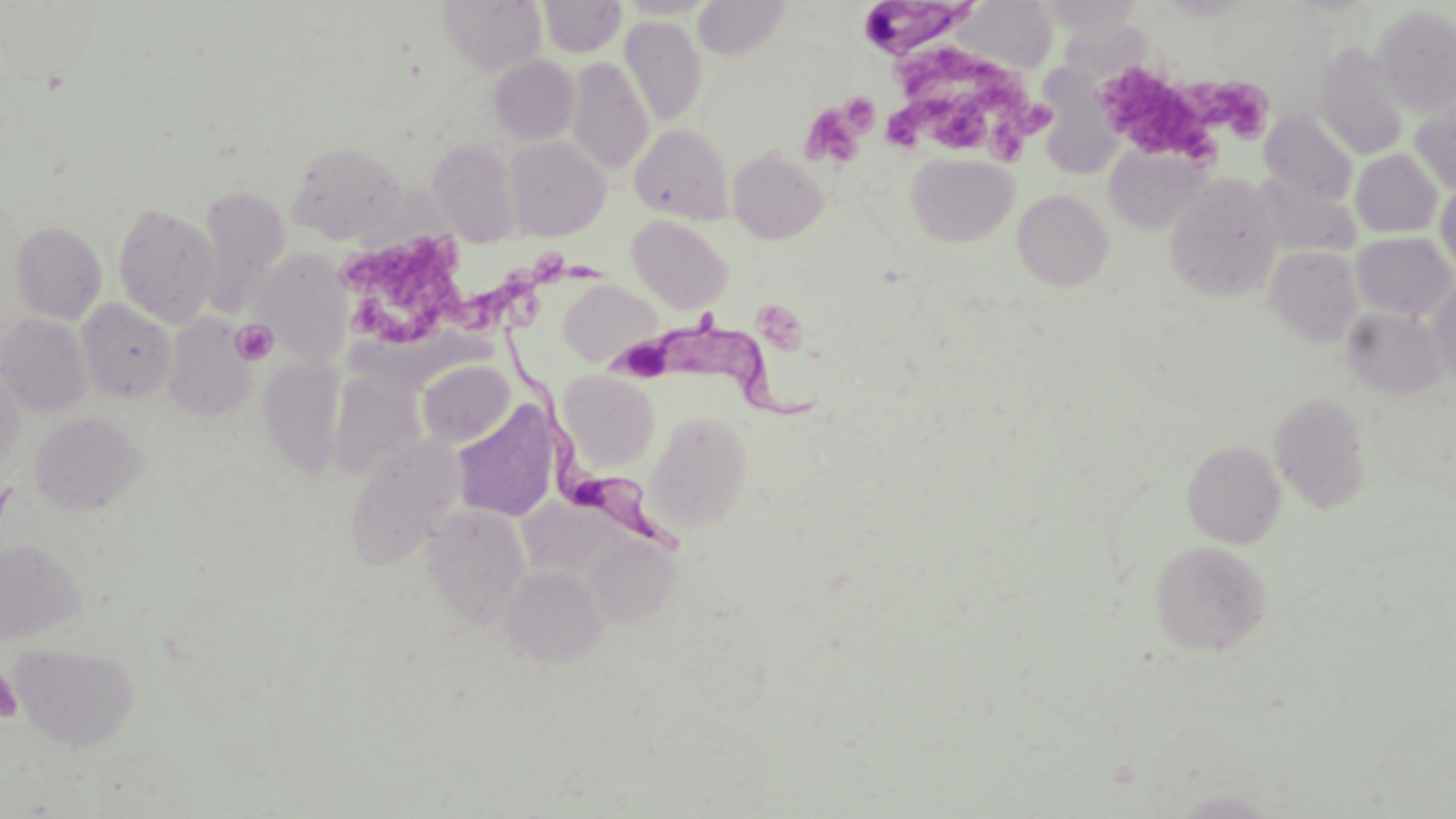
Summary:
  - Coordinate format: approximate bounding boxes as named x1/y1/x2/y2 corners in pixels
  - Uninfected red blood cell locations: (x1=439, y1=0, x2=546, y2=74), (x1=538, y1=0, x2=627, y2=57), (x1=617, y1=0, x2=719, y2=18), (x1=693, y1=0, x2=793, y2=60), (x1=958, y1=0, x2=1057, y2=74), (x1=1039, y1=0, x2=1144, y2=34), (x1=1373, y1=6, x2=1456, y2=116), (x1=620, y1=17, x2=707, y2=125), (x1=1315, y1=44, x2=1409, y2=159), (x1=489, y1=56, x2=580, y2=144), (x1=566, y1=57, x2=654, y2=175), (x1=1039, y1=62, x2=1130, y2=178), (x1=1411, y1=98, x2=1456, y2=193), (x1=1261, y1=110, x2=1359, y2=206), (x1=630, y1=124, x2=734, y2=223), (x1=504, y1=136, x2=610, y2=241), (x1=428, y1=138, x2=522, y2=248), (x1=286, y1=140, x2=408, y2=243), (x1=1105, y1=144, x2=1210, y2=234), (x1=728, y1=148, x2=828, y2=243), (x1=1351, y1=149, x2=1443, y2=237), (x1=907, y1=154, x2=1018, y2=246), (x1=1254, y1=172, x2=1360, y2=257), (x1=1165, y1=174, x2=1282, y2=301), (x1=1435, y1=182, x2=1456, y2=277), (x1=198, y1=185, x2=290, y2=313), (x1=1013, y1=190, x2=1113, y2=291), (x1=112, y1=201, x2=221, y2=328), (x1=627, y1=215, x2=733, y2=314), (x1=10, y1=221, x2=107, y2=324), (x1=1352, y1=232, x2=1455, y2=320), (x1=1265, y1=246, x2=1364, y2=346), (x1=251, y1=248, x2=353, y2=368), (x1=1428, y1=277, x2=1456, y2=389), (x1=560, y1=279, x2=663, y2=367), (x1=77, y1=298, x2=177, y2=402), (x1=1341, y1=307, x2=1448, y2=399), (x1=0, y1=313, x2=93, y2=416), (x1=163, y1=314, x2=257, y2=421), (x1=258, y1=356, x2=345, y2=478), (x1=417, y1=359, x2=514, y2=447), (x1=0, y1=363, x2=25, y2=475), (x1=328, y1=370, x2=425, y2=480), (x1=558, y1=370, x2=660, y2=471), (x1=1269, y1=391, x2=1372, y2=513), (x1=452, y1=402, x2=561, y2=522), (x1=646, y1=409, x2=752, y2=532), (x1=30, y1=412, x2=146, y2=515), (x1=344, y1=435, x2=465, y2=571), (x1=1182, y1=440, x2=1286, y2=549), (x1=423, y1=504, x2=532, y2=627), (x1=585, y1=534, x2=681, y2=626), (x1=0, y1=538, x2=85, y2=644), (x1=1150, y1=540, x2=1271, y2=655), (x1=501, y1=565, x2=607, y2=667), (x1=10, y1=642, x2=140, y2=751), (x1=1168, y1=790, x2=1280, y2=818)
  - Platelet locations: (x1=892, y1=47, x2=983, y2=96), (x1=981, y1=62, x2=1051, y2=161), (x1=1102, y1=65, x2=1216, y2=167), (x1=1192, y1=77, x2=1273, y2=143), (x1=840, y1=91, x2=879, y2=134), (x1=934, y1=93, x2=996, y2=148), (x1=890, y1=94, x2=950, y2=148), (x1=802, y1=104, x2=864, y2=167), (x1=331, y1=229, x2=470, y2=351), (x1=534, y1=251, x2=609, y2=290), (x1=468, y1=269, x2=546, y2=334), (x1=231, y1=319, x2=278, y2=365), (x1=0, y1=666, x2=24, y2=725)
  - Trypanosoma brucei locations: (x1=865, y1=2, x2=985, y2=58), (x1=610, y1=316, x2=824, y2=424), (x1=500, y1=325, x2=688, y2=560)
  - Slide-level diagnosis: Trypanosoma brucei
  - Magnification: 1000x
  - Image size: 1456×819 pixels
  - Field of view: one of a larger specimen
  - Stain: May-Grünwald-Giemsa
  - Modality: light microscopy
  - Preparation: thin blood smear